Report the malaria status of this cell.
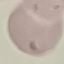

Uninfected.

image type = cell patch, automatically extracted from a larger field of view and resized to 64 × 64 pixels
capture = smartphone through the microscope eyepiece
stain = Giemsa
preparation = thin smear